Locate every blood parasite and identify its species.
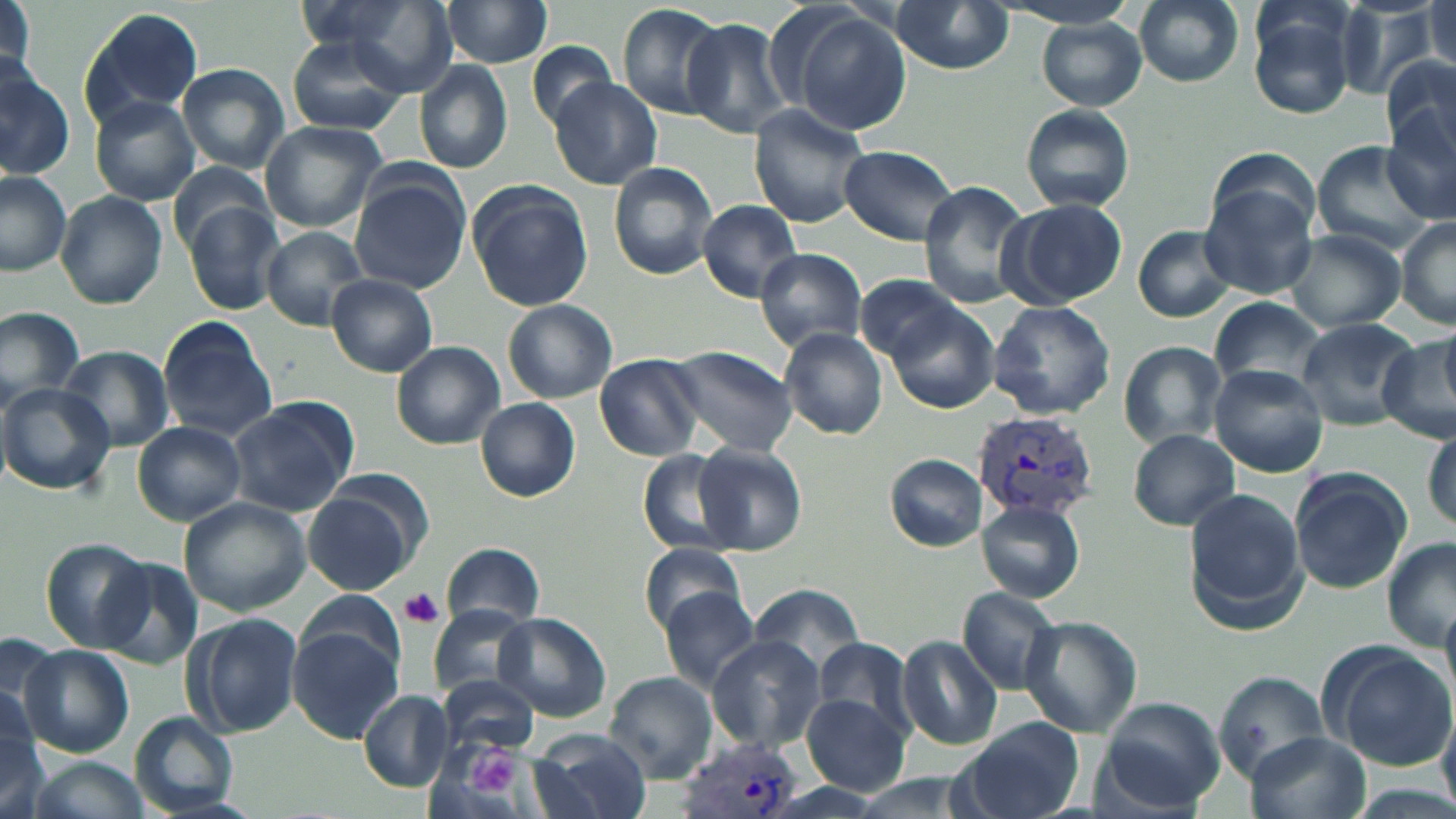

Approximate bounding boxes as [x1, y1, x2, y2] in pixels.
Plasmodium vivax-infected red blood cells: [971, 409, 1097, 522], [676, 738, 800, 819].
No Plasmodium falciparum, Plasmodium ovale, Plasmodium malariae, Babesia divergens, or Trypanosoma brucei observed.

Summary:
  - Uninfected red blood cell locations: [0, 0, 43, 92], [294, 0, 421, 61], [440, 0, 555, 68], [1133, 0, 1245, 87], [1426, 0, 1456, 77], [996, 1, 1143, 29], [890, 2, 1015, 72], [314, 3, 457, 101], [1244, 3, 1362, 118], [617, 4, 731, 119], [79, 5, 204, 123], [1339, 6, 1442, 99], [784, 8, 913, 136], [681, 17, 793, 139], [1037, 17, 1147, 109], [286, 36, 408, 136], [526, 42, 620, 132], [1382, 55, 1456, 156], [415, 61, 513, 175], [177, 63, 289, 173], [0, 65, 75, 180], [550, 76, 662, 190], [88, 96, 199, 205], [749, 104, 873, 228], [1022, 104, 1134, 214], [1381, 116, 1456, 226], [260, 121, 384, 231], [1312, 143, 1431, 251], [841, 146, 960, 245], [1207, 147, 1320, 241], [609, 162, 718, 280], [166, 163, 277, 250], [0, 171, 72, 276], [348, 174, 470, 293], [917, 181, 1033, 307], [468, 182, 593, 313], [1199, 184, 1317, 300], [55, 191, 168, 310], [1002, 197, 1128, 308], [696, 200, 802, 303], [184, 204, 284, 314], [1394, 217, 1456, 328], [1133, 224, 1236, 322], [260, 226, 368, 329], [1284, 230, 1406, 332], [753, 247, 868, 354], [855, 274, 965, 365], [326, 275, 439, 376], [1210, 296, 1328, 395], [501, 299, 617, 403], [986, 300, 1117, 420], [0, 306, 86, 407], [884, 306, 996, 414], [156, 317, 279, 438], [1293, 318, 1418, 427], [1439, 324, 1456, 413], [779, 328, 888, 439], [1378, 333, 1456, 444], [1117, 340, 1227, 449], [391, 342, 505, 449], [58, 345, 174, 450], [664, 345, 799, 457], [594, 355, 704, 462], [1209, 364, 1328, 477], [0, 383, 115, 496], [226, 397, 358, 516], [476, 399, 580, 503], [133, 422, 245, 524], [1424, 428, 1455, 532], [1129, 430, 1239, 529], [692, 441, 808, 555], [638, 449, 744, 555], [883, 455, 986, 551], [1288, 470, 1411, 594], [303, 487, 418, 596], [1181, 487, 1308, 632], [180, 497, 310, 615], [976, 498, 1086, 603], [41, 540, 153, 651], [1382, 540, 1455, 652], [639, 543, 746, 631], [443, 544, 545, 631], [97, 556, 206, 671], [750, 584, 866, 680], [957, 586, 1063, 693], [657, 587, 761, 692], [429, 604, 534, 699], [493, 611, 612, 723], [185, 613, 304, 739], [1020, 617, 1140, 735], [290, 623, 400, 744], [2, 634, 62, 716], [813, 634, 916, 740], [707, 635, 825, 752], [897, 635, 1004, 750], [19, 646, 134, 757], [1328, 646, 1456, 771], [1213, 671, 1328, 780], [606, 672, 718, 780], [438, 678, 536, 758], [359, 692, 453, 793], [802, 694, 910, 794], [1094, 698, 1227, 815], [1438, 705, 1456, 810], [0, 709, 49, 816], [130, 712, 241, 816], [953, 718, 1087, 819], [528, 730, 653, 819], [1245, 731, 1373, 819], [21, 756, 154, 819]
  - Platelet locations: [398, 586, 445, 629], [468, 746, 518, 796]
  - Slide-level diagnosis: Plasmodium vivax
  - Magnification: 1000x
  - Preparation: thin blood smear
  - Field of view: one of a larger specimen
  - Image size: 1456×819 pixels
  - Modality: optical microscopy
  - Stain: May-Grünwald-Giemsa